Classify this cell by malaria status.
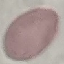
Uninfected.

{
  "image_type": "automatically extracted cell patch, resized to 64 × 64 pixels",
  "stain": "Giemsa",
  "preparation": "thin smear",
  "capture": "smartphone camera at the microscope eyepiece"
}